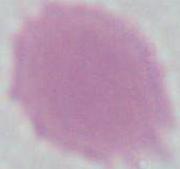

Micrograph. A red blood cell is seen. 1000x magnification.